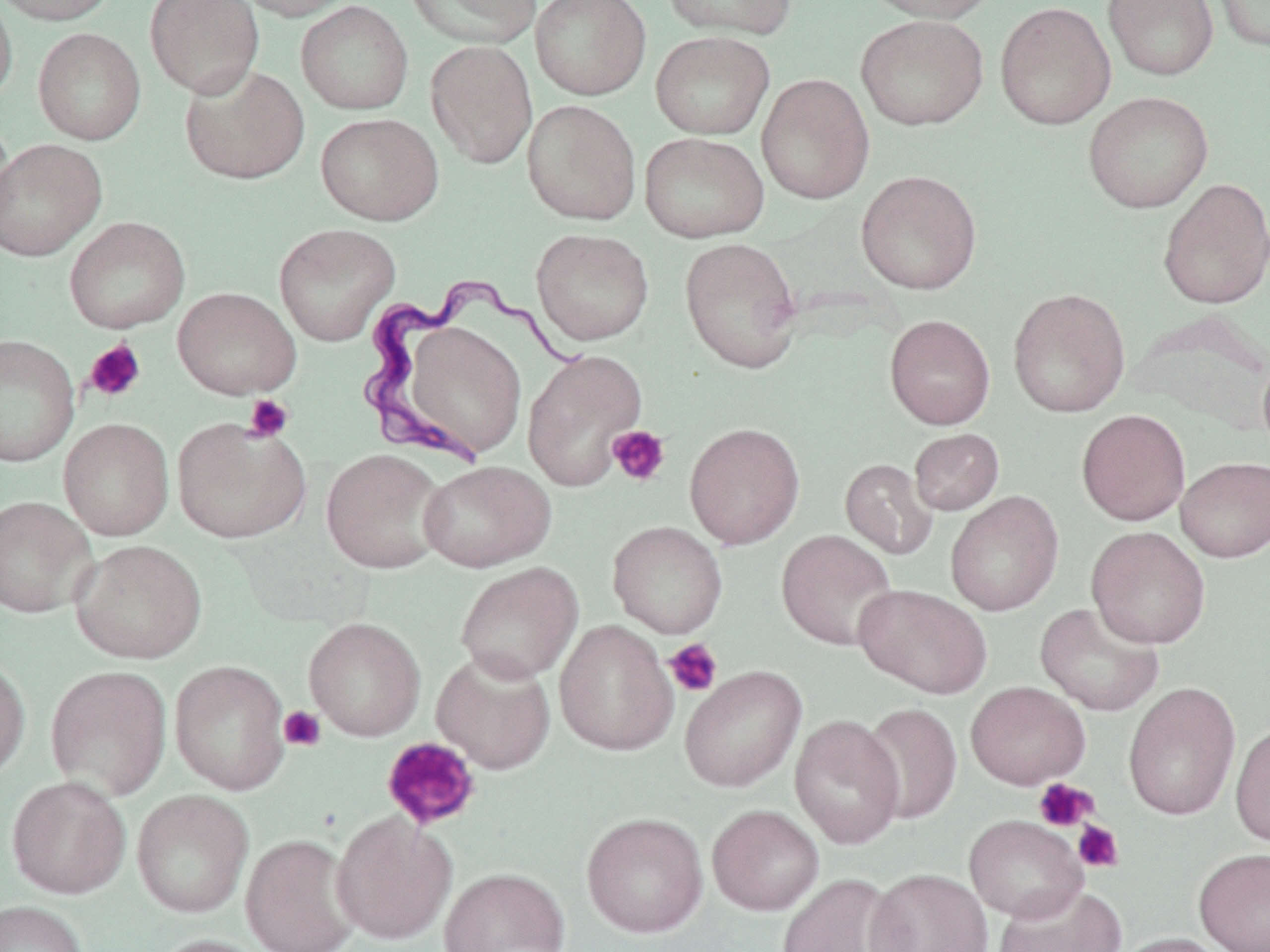

slide-level diagnosis = Trypanosoma brucei
preparation = thin blood film
stain = May-Grünwald-Giemsa
magnification = 1000x
modality = optical microscopy
field of view = one of a larger specimen
uninfected red blood cell locations = approximate bounding boxes as [x1, y1, x2, y2] in pixels: [0, 0, 118, 26], [0, 0, 17, 107], [144, 0, 265, 98], [232, 0, 360, 21], [402, 0, 542, 48], [530, 0, 652, 101], [660, 0, 796, 41], [859, 0, 998, 23], [1102, 0, 1219, 82], [1211, 0, 1270, 54], [995, 1, 1116, 130], [295, 2, 414, 115], [855, 14, 989, 131], [33, 28, 146, 145], [650, 30, 775, 140], [425, 39, 538, 169], [179, 64, 310, 185], [756, 73, 875, 204], [1082, 91, 1214, 213], [522, 99, 642, 225], [315, 112, 444, 226], [0, 116, 15, 242], [638, 131, 770, 243], [0, 139, 107, 261], [856, 170, 982, 294], [1157, 177, 1270, 310], [64, 216, 190, 334], [273, 223, 401, 346], [531, 228, 654, 345], [679, 237, 803, 373], [173, 287, 301, 399], [1008, 288, 1130, 418], [1131, 310, 1270, 433], [884, 314, 995, 429], [387, 315, 534, 463], [0, 334, 80, 467], [522, 349, 646, 490], [1257, 351, 1270, 460], [1076, 409, 1190, 526], [171, 416, 311, 544], [59, 418, 174, 540], [684, 422, 805, 550], [909, 428, 1004, 515], [320, 448, 450, 574], [1175, 456, 1270, 562], [839, 458, 938, 560], [418, 460, 555, 572], [945, 490, 1064, 616], [0, 496, 97, 618], [607, 520, 728, 639], [1086, 526, 1210, 649], [776, 529, 899, 651], [70, 539, 206, 664], [455, 562, 583, 684], [854, 584, 992, 698], [1034, 602, 1165, 717], [303, 617, 426, 741], [554, 620, 679, 756], [431, 649, 556, 774], [0, 654, 31, 781], [169, 660, 290, 795], [44, 664, 172, 800], [679, 665, 807, 792], [966, 681, 1090, 789], [1123, 681, 1241, 821], [859, 702, 963, 824], [790, 714, 905, 849], [1230, 719, 1270, 848], [6, 776, 130, 899], [131, 789, 254, 919], [707, 805, 824, 915], [331, 811, 456, 945], [581, 812, 708, 938], [964, 815, 1087, 922], [241, 834, 361, 952], [1193, 847, 1270, 952], [439, 867, 570, 952], [866, 868, 994, 952], [776, 873, 908, 952], [991, 884, 1127, 952], [0, 900, 88, 952], [1111, 932, 1234, 952], [147, 933, 271, 952]
Trypanosoma brucei locations = approximate bounding boxes as [x1, y1, x2, y2] in pixels: [352, 278, 586, 466]
image size = 1270×952 pixels
platelet locations = approximate bounding boxes as [x1, y1, x2, y2] in pixels: [83, 338, 146, 403], [244, 394, 294, 443], [607, 425, 671, 487], [662, 638, 723, 697], [279, 705, 326, 752], [381, 737, 482, 830], [1033, 778, 1097, 832], [1072, 819, 1124, 873]